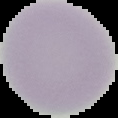

Summary:
  - Image type: segmented cell region on a black background
  - Result: no Plasmodium parasites detected
  - Preparation: thin blood smear
  - Image size: 118×118 pixels